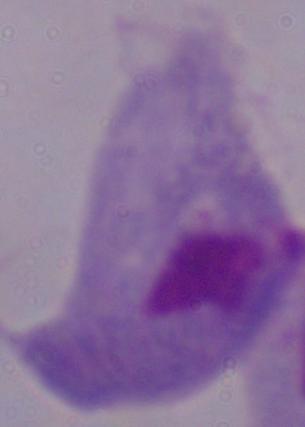
identification = trichomonad
magnification = 1000x
modality = photomicrograph